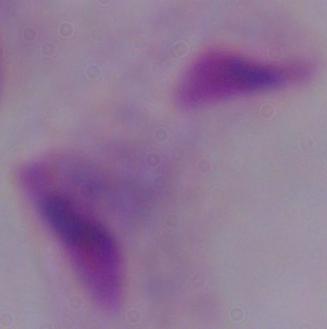

{
  "modality": "micrograph",
  "identification": "trichomonad",
  "magnification": "1000x"
}